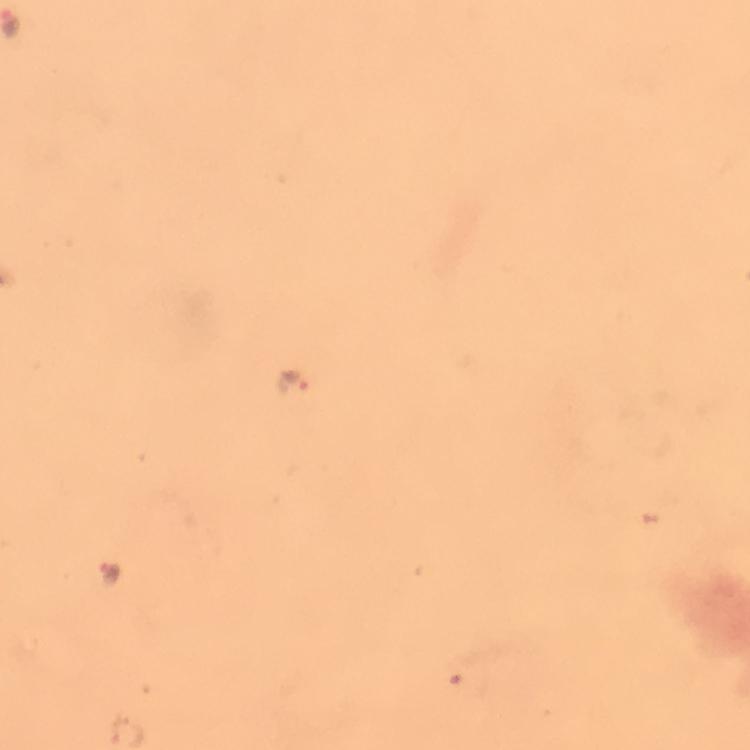

Approximate centers as {x, y} in pixels.
Summary:
  - Plasmodium parasite locations: {289, 380}, {110, 572}
  - Capture: smartphone mounted on the microscope
  - Stain: Giemsa
  - Context: from a diagnostic examination for malaria
  - Magnification: 100x
  - Image size: 750×750 pixels
  - Cropped from: one field of view
  - Preparation: thick blood film
  - Immersion oil: used